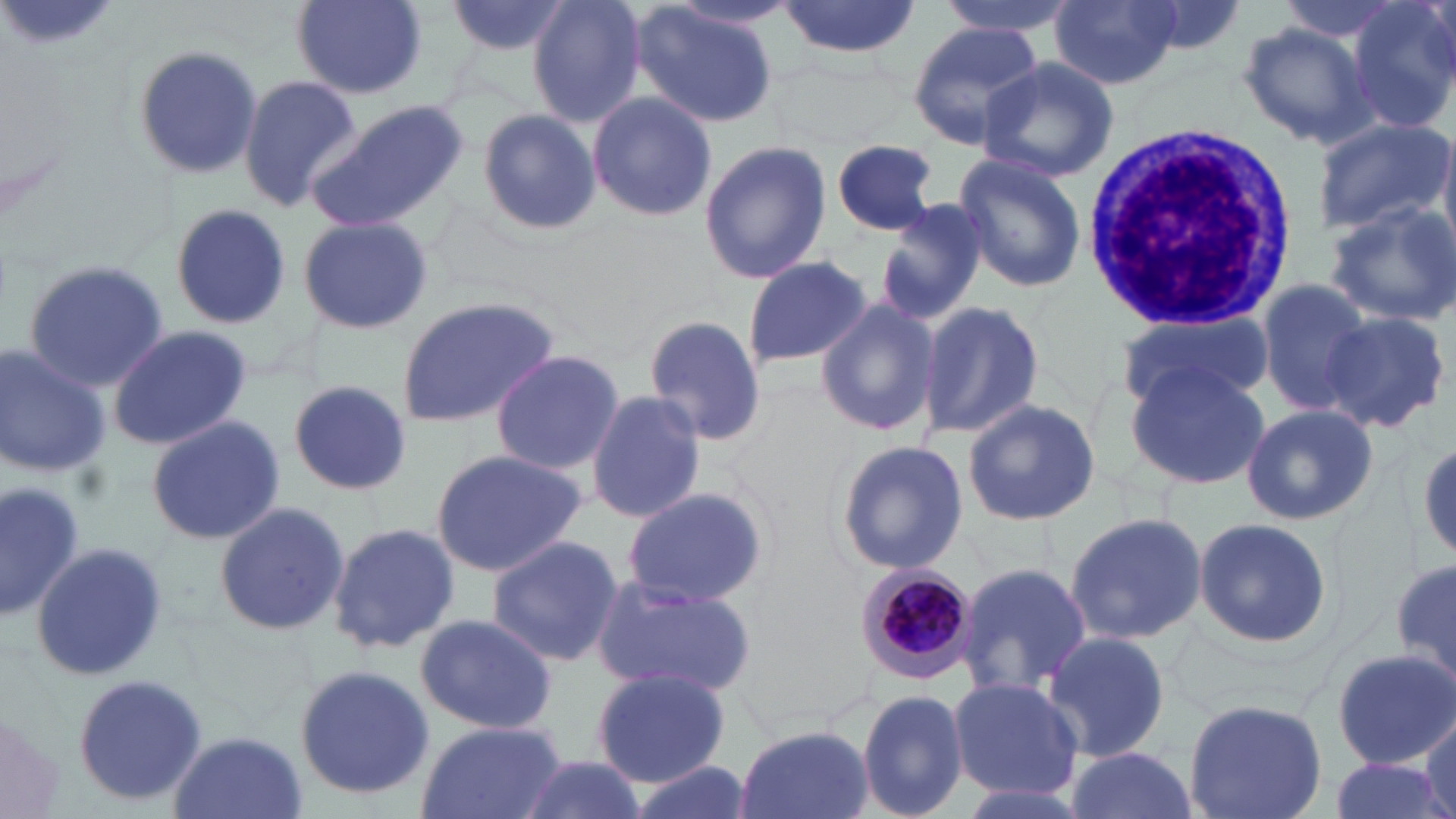
Summary:
  - Coordinate format: approximate bounding boxes as (x1,y1)-(x2,y2) corner pairs in pixels
  - Plasmodium malariae-infected red blood cell locations: (856,563)-(977,685)
  - Uninfected red blood cell locations: (444,0)-(574,59), (527,0)-(648,128), (776,0)-(920,59), (930,0)-(1080,39), (1048,0)-(1182,91), (292,1)-(426,99), (1348,1)-(1456,136), (630,3)-(778,127), (1235,20)-(1377,148), (905,22)-(1042,151), (128,44)-(264,183), (977,57)-(1118,182), (237,74)-(362,213), (586,92)-(719,221), (307,102)-(470,234), (477,106)-(599,237), (1311,117)-(1452,236), (698,138)-(832,286), (830,139)-(943,235), (952,153)-(1088,292), (873,200)-(991,325), (1324,201)-(1456,326), (170,202)-(291,328), (298,215)-(435,337), (741,256)-(872,369), (20,261)-(175,393), (1254,276)-(1378,416), (394,297)-(561,429), (916,300)-(1044,440), (814,301)-(941,438), (1116,307)-(1273,413), (1323,311)-(1450,433), (644,316)-(765,445), (106,323)-(254,453), (0,343)-(109,478), (489,350)-(625,474), (1125,363)-(1269,488), (288,380)-(410,498), (586,388)-(705,526), (962,398)-(1099,526), (1239,403)-(1377,526), (144,416)-(285,545), (834,438)-(969,576), (1415,438)-(1455,563), (426,448)-(588,577), (0,479)-(87,621), (620,486)-(769,607), (213,501)-(349,640), (1063,511)-(1207,646), (1192,516)-(1332,650), (327,523)-(460,653), (485,534)-(624,668), (29,542)-(171,687), (1392,558)-(1456,688), (952,561)-(1092,695), (591,575)-(754,697), (413,612)-(559,736), (1041,630)-(1174,763), (1331,647)-(1456,769), (293,664)-(435,801), (590,667)-(731,787), (70,674)-(210,806), (946,677)-(1084,802), (857,690)-(969,819), (1183,698)-(1326,819), (1421,705)-(1456,819), (0,711)-(69,819), (416,721)-(564,819), (734,725)-(874,819), (169,731)-(307,819), (1060,745)-(1198,819), (510,753)-(651,819), (1327,757)-(1452,819), (624,760)-(755,819), (947,778)-(1096,819)
  - White blood cell locations: (1080,119)-(1296,342)
  - Slide-level diagnosis: Plasmodium malariae
  - Stain: May-Grünwald-Giemsa
  - Modality: optical microscopy
  - Image size: 1456×819 pixels
  - Preparation: thin blood smear
  - Field of view: single
  - Magnification: 1000x